Give the position of every leukocyte visible.
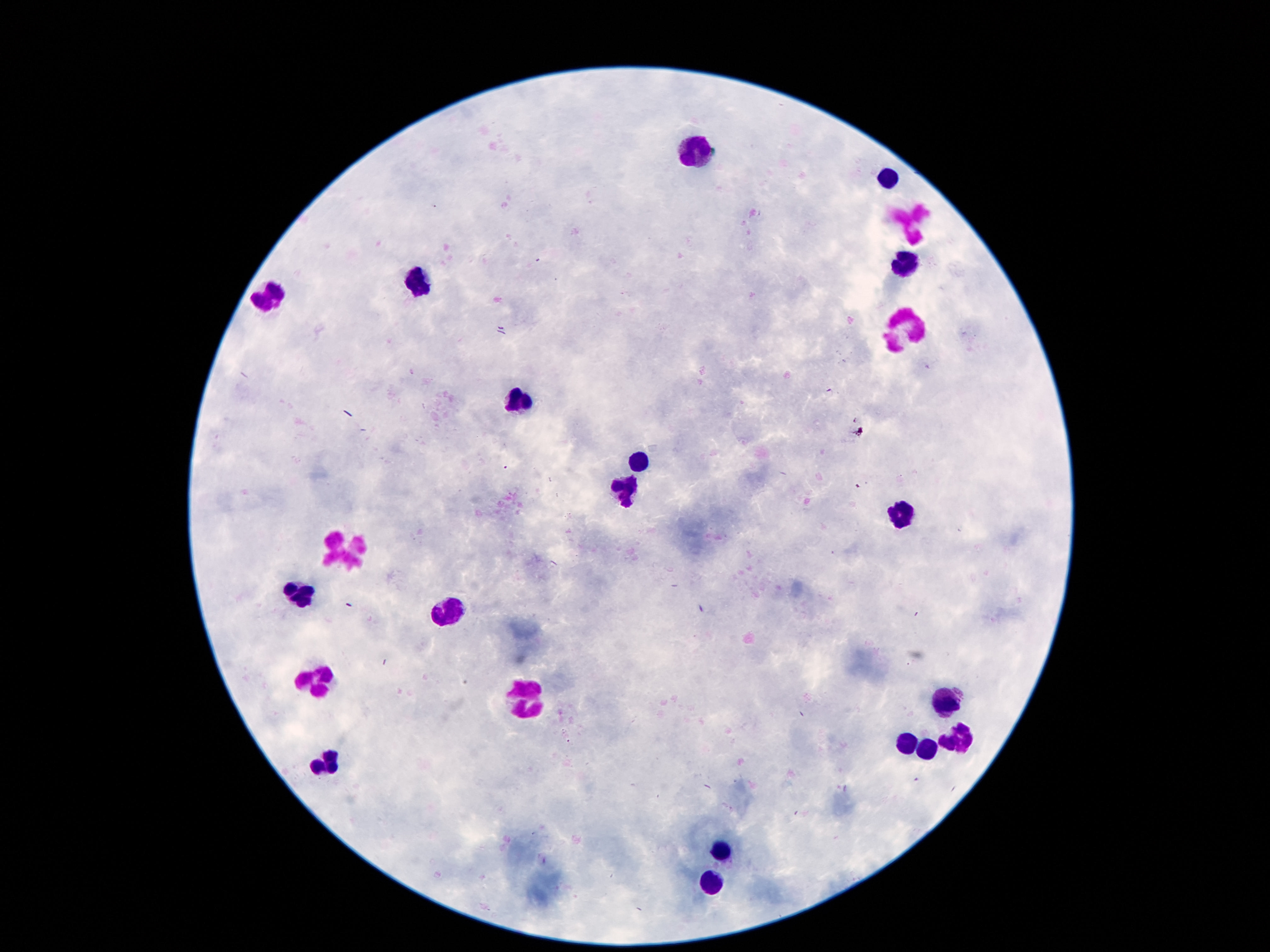

Approximate centers as {x, y} in pixels.
Leukocytes: {699, 150}, {888, 178}, {911, 221}, {903, 265}, {418, 285}, {267, 295}, {901, 327}, {519, 398}, {632, 465}, {628, 482}, {901, 514}, {344, 554}, {300, 593}, {447, 610}, {317, 678}, {523, 698}, {947, 699}, {957, 734}, {907, 742}, {928, 746}, {325, 763}, {720, 851}, {712, 885}.

Single field of view. Giemsa stain. Photographed through the microscope eyepiece with a smartphone camera. 100x magnification. Patient malaria status: uninfected. Image is 1270×952 pixels. Thick blood film.